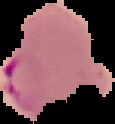
From a thin blood film. Cell region segmented out of the field of view; the surrounding area is masked to black. Malaria status: parasitized. Image is 115×124 pixels.